State the preparation type.
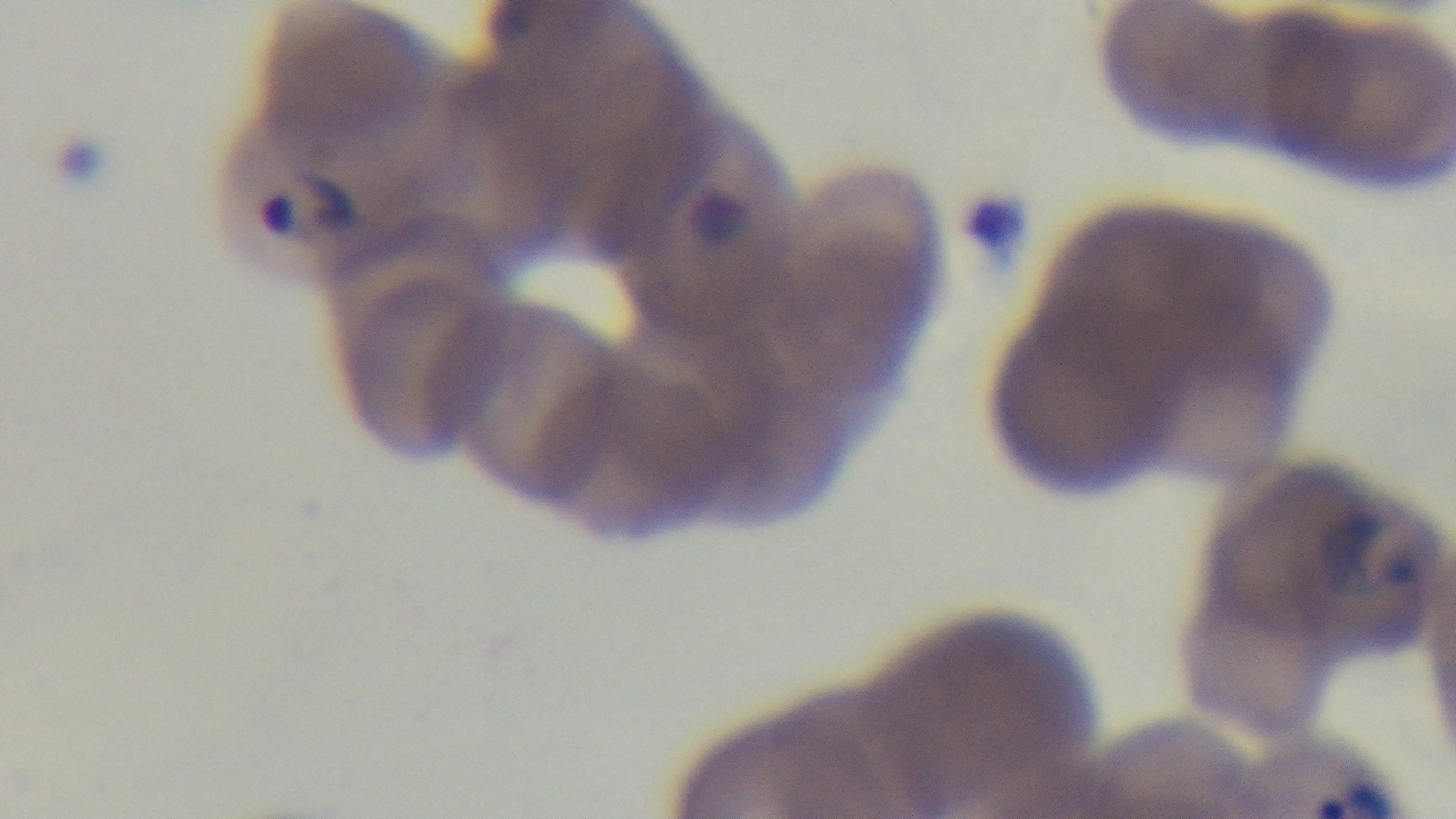

Thin.

Summary:
  - Malaria status: infected
  - Stain: Giemsa
  - Modality: light microscopy
  - Field of view: one from the slide
  - Objective: 100x oil immersion
  - Capture: mounted 4K digital camera